Give the position of every malaria parasite.
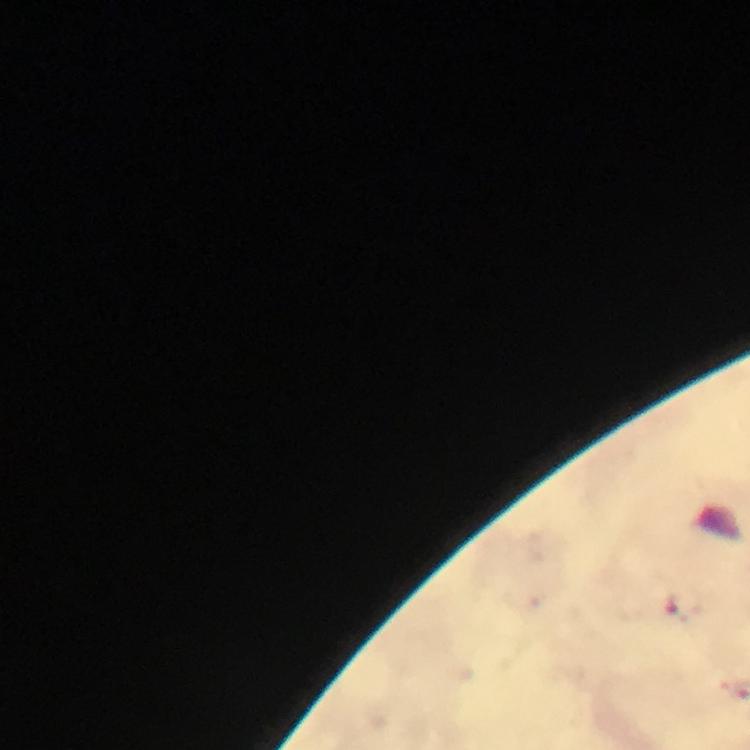
Approximate centers as (x, y) in pixels.
Malaria parasites: (683, 604).

{
  "stain": "Giemsa",
  "preparation": "thick blood smear",
  "cropped_from": "one field of view",
  "image_size": "750×750 pixels",
  "capture": "smartphone mounted on the microscope",
  "context": "from a diagnostic examination for malaria",
  "immersion_oil": "applied",
  "magnification": "100x"
}